Describe the morphology of the erythrocytes.
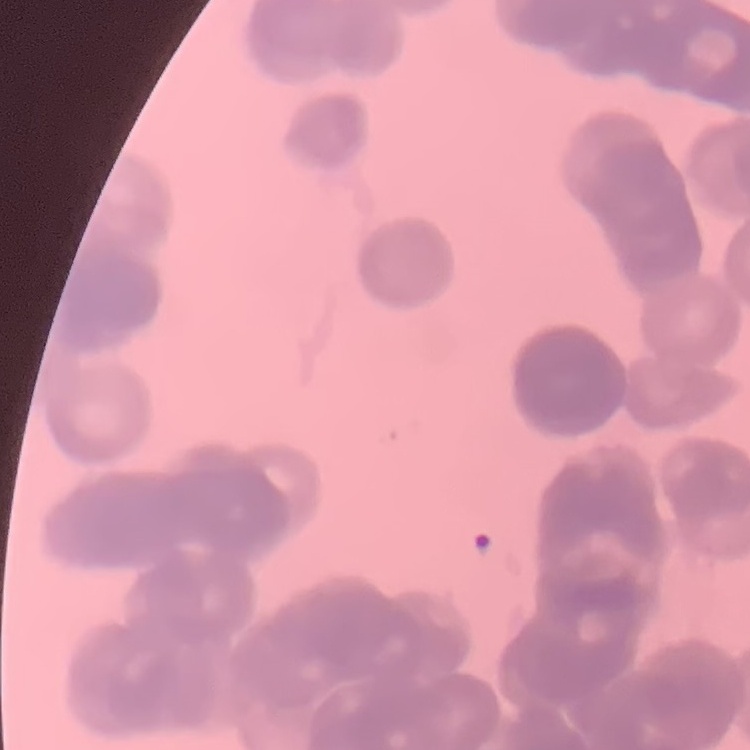
They show rouleaux formation.

Field's or Giemsa stain. Thin blood smear. Square crop of a larger photomicrograph.